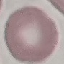
Summary:
  - Result: negative for malaria parasites
  - Image type: automatically extracted cell patch, resized to 64 × 64 pixels
  - Capture: smartphone through the microscope eyepiece
  - Preparation: thin blood smear
  - Stain: Giemsa